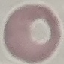
Summary:
  - Malaria status: uninfected
  - Preparation: thin smear
  - Stain: Giemsa
  - Capture: smartphone camera at the microscope eyepiece
  - Image type: cell patch, automatically extracted from a larger field of view and resized to 64 × 64 pixels